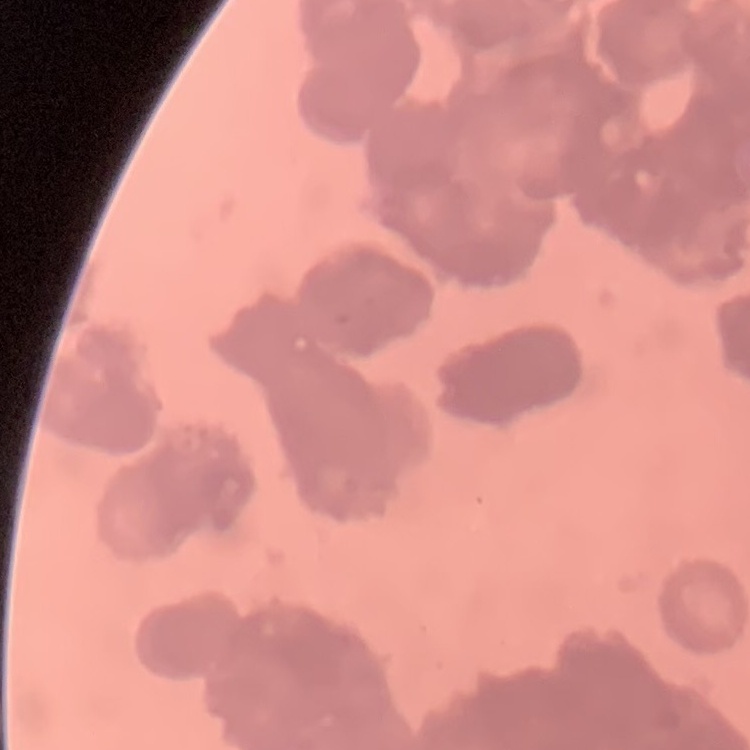
Summary:
  - Erythrocyte morphology: rouleaux formation
  - Preparation: thin peripheral smear
  - Stain: Field's or Giemsa
  - Image type: square crop of a larger photomicrograph